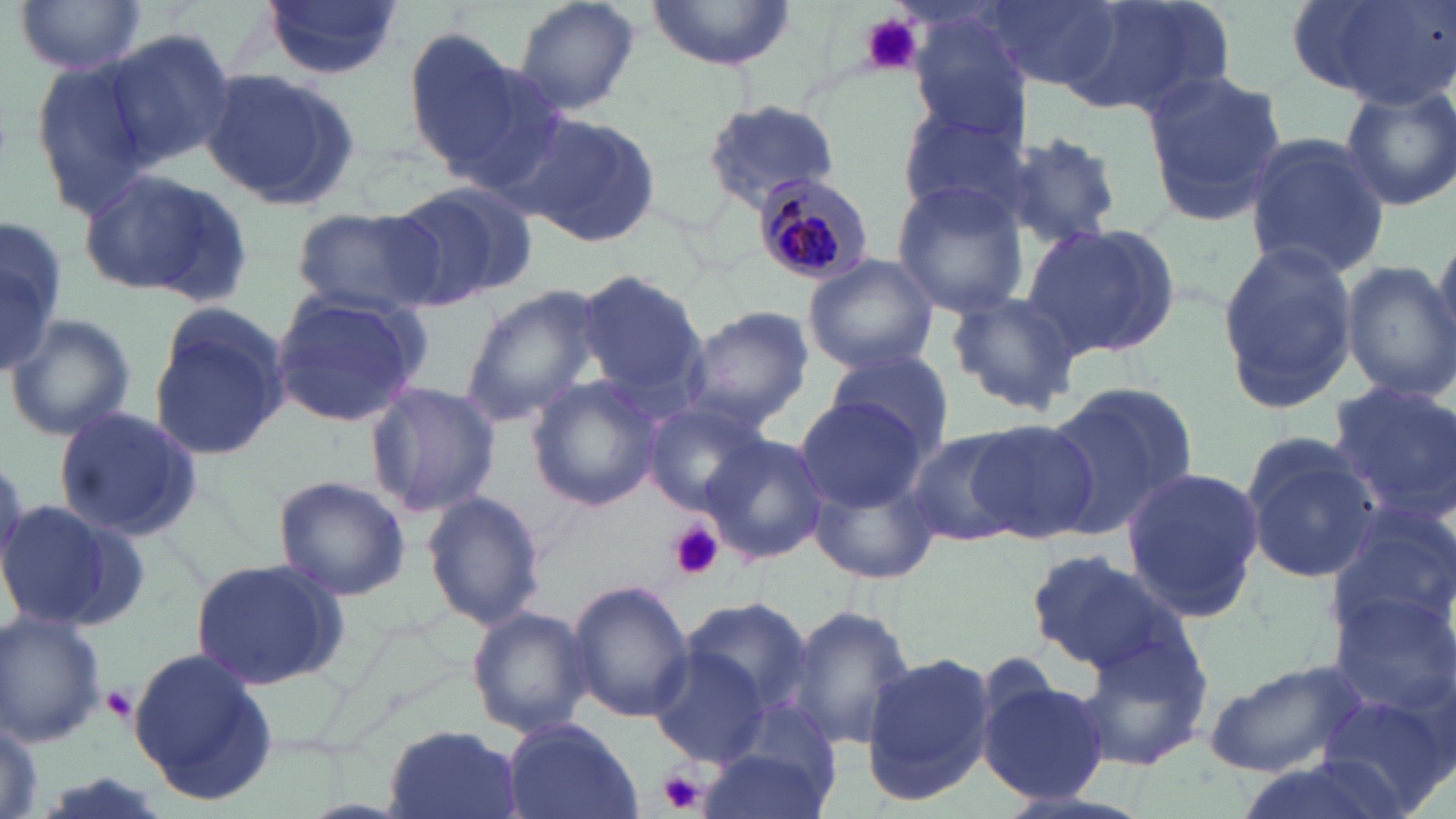
Approximate bounding boxes as (x1, y1, x2, y2) in pixels. Uninfected red blood cell locations: (12, 0, 149, 76), (260, 0, 401, 79), (511, 0, 643, 118), (646, 0, 796, 71), (983, 0, 1134, 90), (1067, 0, 1238, 121), (1288, 1, 1452, 107), (905, 9, 1033, 139), (401, 27, 524, 166), (103, 28, 235, 168), (29, 57, 164, 214), (432, 59, 575, 195), (202, 69, 363, 210), (1140, 69, 1286, 222), (1339, 81, 1456, 212), (701, 100, 841, 209), (896, 103, 1029, 223), (512, 112, 662, 249), (999, 131, 1124, 248), (1242, 133, 1391, 279), (80, 165, 254, 302), (389, 179, 530, 309), (888, 182, 1030, 317), (290, 204, 444, 316), (0, 217, 64, 373), (1428, 222, 1456, 356), (1023, 224, 1181, 360), (1215, 242, 1358, 410), (801, 254, 941, 374), (1341, 260, 1455, 401), (573, 269, 705, 399), (459, 288, 604, 427), (268, 290, 429, 428), (945, 291, 1080, 415), (147, 303, 290, 461), (684, 305, 814, 430), (5, 313, 139, 441), (823, 349, 953, 455), (525, 376, 664, 512), (363, 379, 502, 519), (1044, 382, 1195, 539), (1327, 383, 1456, 518), (793, 396, 927, 513), (641, 401, 765, 517), (53, 406, 204, 544), (966, 419, 1102, 542), (900, 428, 1029, 546), (701, 433, 831, 566), (1242, 436, 1381, 584), (1119, 467, 1266, 620), (809, 471, 941, 585), (272, 475, 410, 603), (420, 490, 545, 631), (0, 498, 140, 632), (1325, 499, 1455, 657), (1026, 548, 1187, 675), (190, 557, 350, 688), (567, 580, 695, 725), (1328, 587, 1456, 721), (680, 594, 814, 718), (785, 601, 918, 756), (467, 608, 595, 738), (0, 612, 107, 747), (1073, 626, 1214, 772), (648, 645, 771, 766), (128, 648, 278, 807), (861, 651, 996, 804), (1202, 659, 1368, 778), (979, 671, 1110, 807), (1317, 689, 1452, 819), (0, 716, 45, 817), (503, 717, 644, 819), (383, 726, 523, 819), (696, 738, 837, 819). Plasmodium malariae-infected red blood cell locations: (748, 172, 873, 287). Platelet locations: (856, 11, 927, 75), (671, 522, 722, 579), (100, 685, 138, 726), (656, 768, 707, 815). Slide-level diagnosis: Plasmodium malariae. May-Grünwald-Giemsa stain. 1000x magnification. Image is 1456×819 pixels. Light microscopy. Single field of view. Thin blood film.